Comment on the morphology of the erythrocytes.
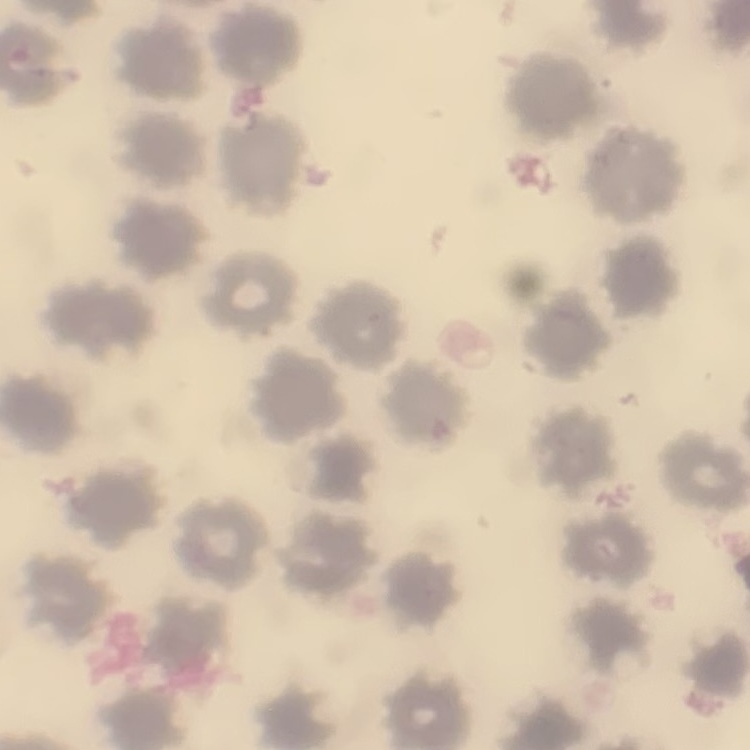
No rouleaux formation.

preparation: thin blood film
stain: Field's or Giemsa
image_type: square crop of a larger photomicrograph